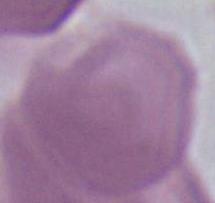
Summary:
  - Identification: erythrocyte
  - Magnification: 1000x
  - Modality: micrograph